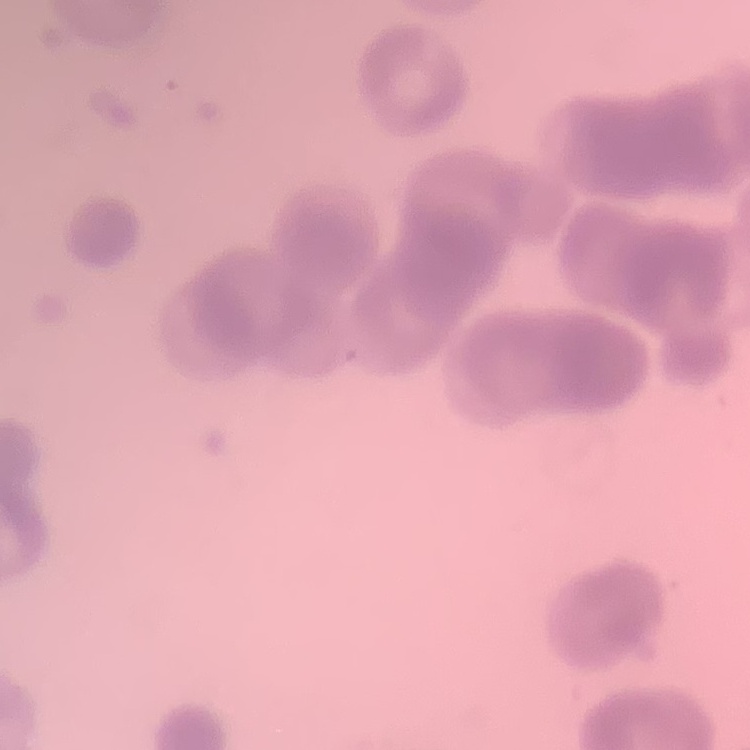
red blood cell morphology = rouleaux formation
preparation = thin blood film
image type = square crop of a larger photomicrograph
stain = Field's or Giemsa